Describe the morphology of the red blood cells.
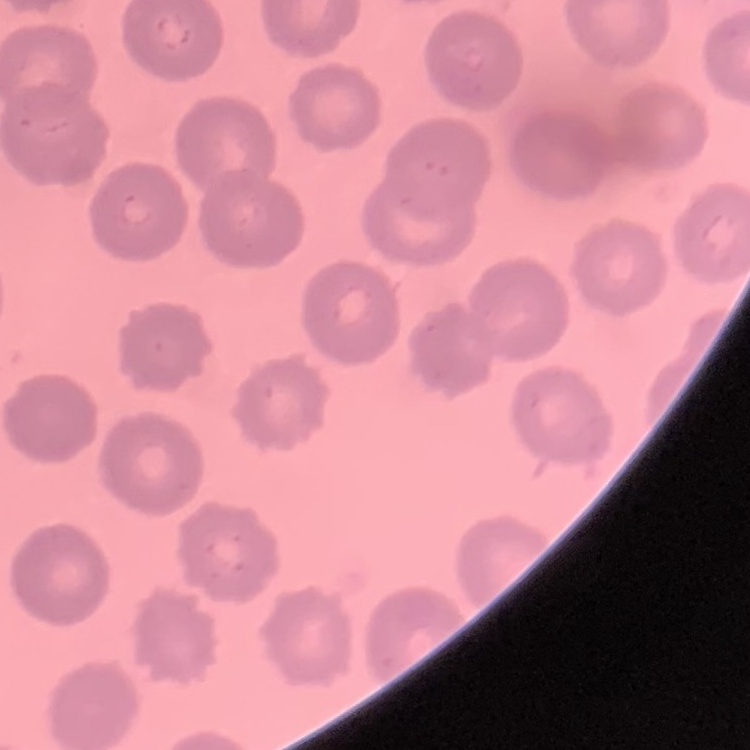
No rouleaux formation.

Thin blood film. Stained with either Field's or Giemsa. One tile cut from a larger photomicrograph.